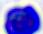
Micrograph. 400x magnification. A leukocyte is shown.